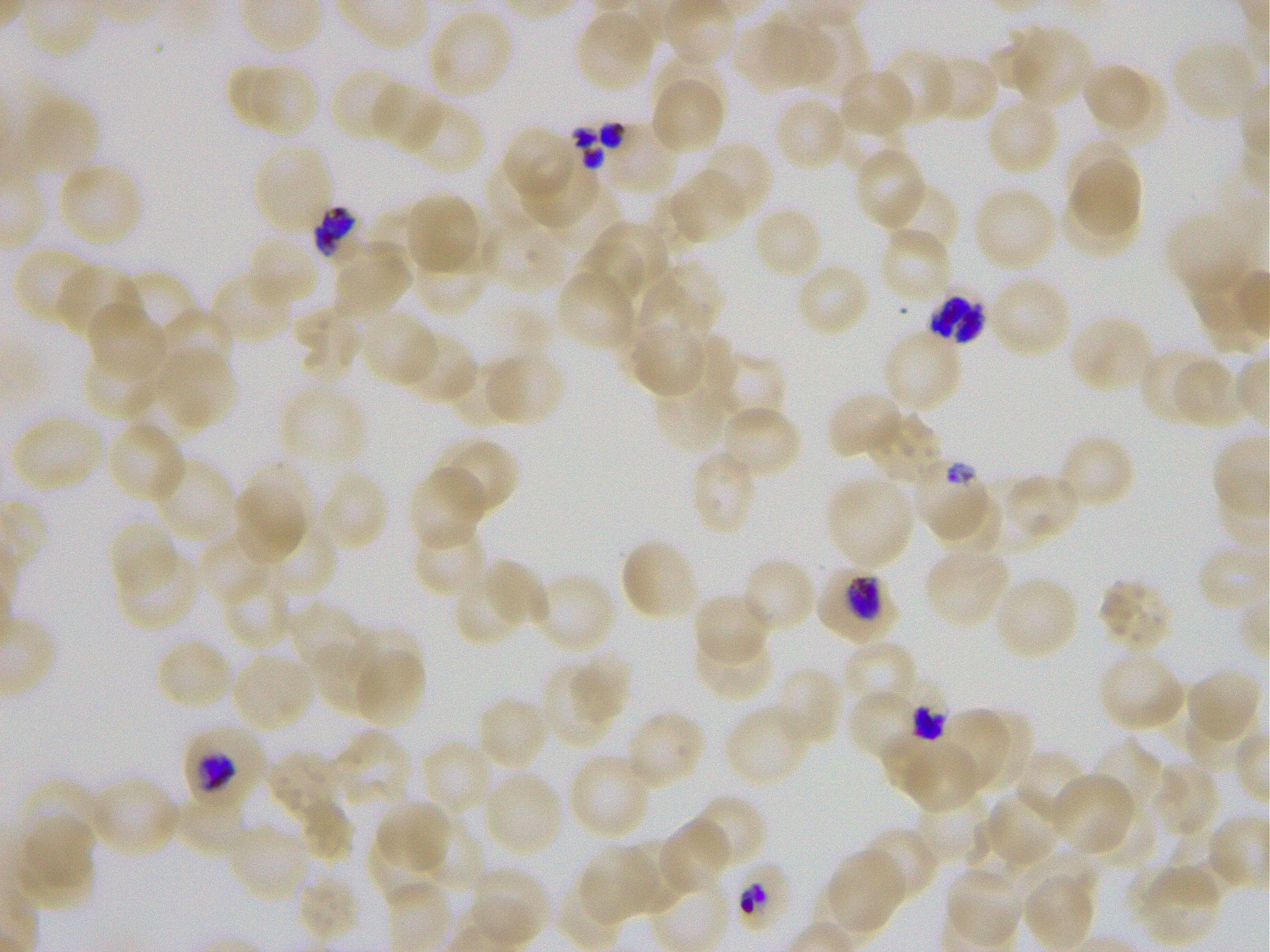

Not every red blood cell is marked. A life-cycle stage — or a range of stages, where the recorded stages span more than one — follows each staged infected red blood cell.
{
  "objective": "100x, oil immersion, numerical aperture 1.25",
  "locations_of_infected_red_blood_cells": "approximate bounding rectangles given as corner coordinates in pixels from the top-left: (x1=315, y1=205, x2=362, y2=263); (x1=924, y1=282, x2=991, y2=350); (x1=913, y1=462, x2=983, y2=542) late ring to early trophozoite; (x1=817, y1=565, x2=899, y2=643) early trophozoite to early schizont; (x1=904, y1=684, x2=951, y2=742) late trophozoite to late schizont; (x1=182, y1=723, x2=267, y2=807) trophozoite; (x1=729, y1=855, x2=799, y2=933)",
  "culture": "Plasmodium falciparum strain 3D7, static, in vitro",
  "preparation": "thin blood film",
  "image_size": "1270×952 pixels",
  "field_of_view": "one from this slide",
  "stain": "Giemsa",
  "locations_of_uninfected_red_blood_cells": "approximate bounding rectangles given as corner coordinates in pixels from the top-left: (x1=427, y1=8, x2=515, y2=101), (x1=574, y1=8, x2=658, y2=93), (x1=803, y1=12, x2=868, y2=95), (x1=732, y1=17, x2=810, y2=93), (x1=760, y1=26, x2=839, y2=84), (x1=988, y1=26, x2=1054, y2=89), (x1=1018, y1=30, x2=1092, y2=110), (x1=1172, y1=38, x2=1262, y2=123), (x1=877, y1=47, x2=954, y2=127), (x1=922, y1=52, x2=999, y2=122), (x1=658, y1=56, x2=727, y2=122), (x1=1084, y1=59, x2=1149, y2=128), (x1=252, y1=66, x2=319, y2=136), (x1=226, y1=67, x2=280, y2=125), (x1=329, y1=68, x2=410, y2=142), (x1=837, y1=68, x2=914, y2=139), (x1=650, y1=71, x2=726, y2=156), (x1=1096, y1=71, x2=1166, y2=146), (x1=369, y1=82, x2=445, y2=152), (x1=772, y1=95, x2=849, y2=172), (x1=985, y1=97, x2=1062, y2=176), (x1=401, y1=99, x2=484, y2=174), (x1=836, y1=110, x2=905, y2=176), (x1=501, y1=125, x2=580, y2=203), (x1=1068, y1=136, x2=1131, y2=200), (x1=252, y1=141, x2=334, y2=237), (x1=694, y1=142, x2=772, y2=223), (x1=854, y1=148, x2=927, y2=229), (x1=486, y1=157, x2=551, y2=229), (x1=518, y1=160, x2=601, y2=229), (x1=1074, y1=160, x2=1141, y2=236), (x1=57, y1=161, x2=145, y2=246), (x1=668, y1=168, x2=748, y2=246), (x1=882, y1=181, x2=959, y2=259), (x1=972, y1=186, x2=1059, y2=273), (x1=1064, y1=190, x2=1135, y2=254), (x1=405, y1=192, x2=484, y2=277), (x1=751, y1=205, x2=824, y2=281), (x1=368, y1=207, x2=435, y2=268), (x1=1164, y1=208, x2=1258, y2=299), (x1=485, y1=220, x2=562, y2=291), (x1=598, y1=220, x2=668, y2=284), (x1=877, y1=227, x2=952, y2=305), (x1=245, y1=233, x2=321, y2=309), (x1=332, y1=241, x2=412, y2=319), (x1=576, y1=242, x2=645, y2=301), (x1=12, y1=245, x2=100, y2=325), (x1=413, y1=251, x2=490, y2=314), (x1=795, y1=260, x2=872, y2=338), (x1=55, y1=263, x2=139, y2=341), (x1=657, y1=264, x2=727, y2=326), (x1=555, y1=267, x2=638, y2=353), (x1=209, y1=269, x2=294, y2=346), (x1=121, y1=270, x2=199, y2=336), (x1=987, y1=274, x2=1072, y2=359), (x1=634, y1=286, x2=711, y2=350), (x1=87, y1=302, x2=169, y2=382), (x1=293, y1=305, x2=365, y2=378), (x1=156, y1=309, x2=235, y2=380), (x1=357, y1=309, x2=439, y2=388), (x1=1068, y1=314, x2=1155, y2=395), (x1=624, y1=320, x2=710, y2=398), (x1=880, y1=327, x2=964, y2=416), (x1=398, y1=331, x2=478, y2=405), (x1=688, y1=333, x2=737, y2=413), (x1=653, y1=336, x2=740, y2=454), (x1=1138, y1=348, x2=1218, y2=426), (x1=81, y1=350, x2=163, y2=419), (x1=480, y1=350, x2=566, y2=427), (x1=719, y1=352, x2=785, y2=427), (x1=164, y1=353, x2=233, y2=424), (x1=1171, y1=355, x2=1249, y2=428), (x1=450, y1=359, x2=515, y2=426), (x1=127, y1=375, x2=211, y2=443), (x1=279, y1=383, x2=366, y2=473), (x1=827, y1=390, x2=906, y2=459), (x1=718, y1=404, x2=803, y2=482), (x1=864, y1=409, x2=945, y2=487), (x1=9, y1=414, x2=105, y2=493), (x1=112, y1=421, x2=188, y2=501), (x1=1057, y1=433, x2=1136, y2=510), (x1=430, y1=436, x2=519, y2=519), (x1=687, y1=449, x2=759, y2=537), (x1=149, y1=456, x2=238, y2=543), (x1=246, y1=459, x2=313, y2=532), (x1=407, y1=467, x2=487, y2=549), (x1=315, y1=468, x2=390, y2=552), (x1=1004, y1=473, x2=1080, y2=539), (x1=824, y1=475, x2=915, y2=571), (x1=977, y1=476, x2=1042, y2=556), (x1=233, y1=486, x2=307, y2=562), (x1=933, y1=489, x2=1000, y2=553), (x1=109, y1=518, x2=181, y2=597), (x1=411, y1=522, x2=491, y2=597), (x1=252, y1=523, x2=339, y2=600), (x1=198, y1=531, x2=273, y2=603), (x1=619, y1=537, x2=701, y2=622), (x1=925, y1=544, x2=1013, y2=628), (x1=117, y1=546, x2=201, y2=632), (x1=740, y1=555, x2=817, y2=635), (x1=485, y1=558, x2=550, y2=626), (x1=221, y1=567, x2=296, y2=650), (x1=531, y1=571, x2=619, y2=654), (x1=992, y1=575, x2=1080, y2=662), (x1=1098, y1=577, x2=1174, y2=653), (x1=457, y1=578, x2=516, y2=644), (x1=692, y1=591, x2=771, y2=667), (x1=288, y1=602, x2=366, y2=681), (x1=355, y1=626, x2=423, y2=690), (x1=691, y1=630, x2=775, y2=701), (x1=313, y1=636, x2=387, y2=718), (x1=155, y1=637, x2=236, y2=711), (x1=840, y1=641, x2=917, y2=717), (x1=1097, y1=646, x2=1186, y2=733), (x1=571, y1=650, x2=633, y2=722), (x1=229, y1=651, x2=317, y2=733), (x1=360, y1=655, x2=424, y2=729), (x1=543, y1=666, x2=611, y2=746), (x1=769, y1=666, x2=843, y2=749), (x1=1185, y1=666, x2=1263, y2=745), (x1=848, y1=693, x2=916, y2=761), (x1=476, y1=695, x2=552, y2=771), (x1=724, y1=702, x2=813, y2=787), (x1=935, y1=707, x2=1008, y2=791), (x1=624, y1=708, x2=706, y2=790), (x1=974, y1=714, x2=1030, y2=788), (x1=1185, y1=714, x2=1256, y2=770), (x1=321, y1=731, x2=412, y2=812), (x1=881, y1=732, x2=983, y2=812), (x1=1090, y1=734, x2=1161, y2=813), (x1=419, y1=739, x2=495, y2=815), (x1=1011, y1=748, x2=1092, y2=823), (x1=567, y1=752, x2=653, y2=841), (x1=269, y1=753, x2=334, y2=821), (x1=1152, y1=761, x2=1221, y2=839), (x1=482, y1=770, x2=564, y2=857), (x1=1049, y1=772, x2=1137, y2=855), (x1=23, y1=774, x2=116, y2=857), (x1=88, y1=774, x2=181, y2=857), (x1=983, y1=788, x2=1066, y2=870), (x1=168, y1=791, x2=248, y2=851), (x1=915, y1=791, x2=986, y2=855), (x1=689, y1=794, x2=767, y2=873), (x1=374, y1=798, x2=455, y2=875), (x1=297, y1=800, x2=356, y2=858), (x1=1092, y1=802, x2=1158, y2=867), (x1=14, y1=813, x2=97, y2=907), (x1=659, y1=817, x2=733, y2=897), (x1=418, y1=819, x2=487, y2=884), (x1=965, y1=820, x2=1027, y2=886), (x1=224, y1=824, x2=311, y2=903), (x1=861, y1=826, x2=939, y2=904), (x1=1173, y1=828, x2=1241, y2=900), (x1=368, y1=834, x2=440, y2=904), (x1=616, y1=838, x2=685, y2=916), (x1=577, y1=844, x2=658, y2=925), (x1=821, y1=850, x2=905, y2=937), (x1=1021, y1=850, x2=1102, y2=897), (x1=642, y1=851, x2=731, y2=945), (x1=1133, y1=864, x2=1224, y2=945), (x1=471, y1=865, x2=550, y2=927), (x1=943, y1=865, x2=1024, y2=948), (x1=298, y1=875, x2=360, y2=943), (x1=1024, y1=875, x2=1092, y2=947), (x1=470, y1=895, x2=539, y2=944)",
  "donor_blood_group": "O+"
}